Report the malaria status of this cell.
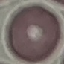

It is uninfected.

Summary:
  - Stain: Giemsa
  - Image type: automatically extracted cell patch, resized to 64 × 64 pixels
  - Capture: smartphone camera at the microscope eyepiece
  - Preparation: thin blood film